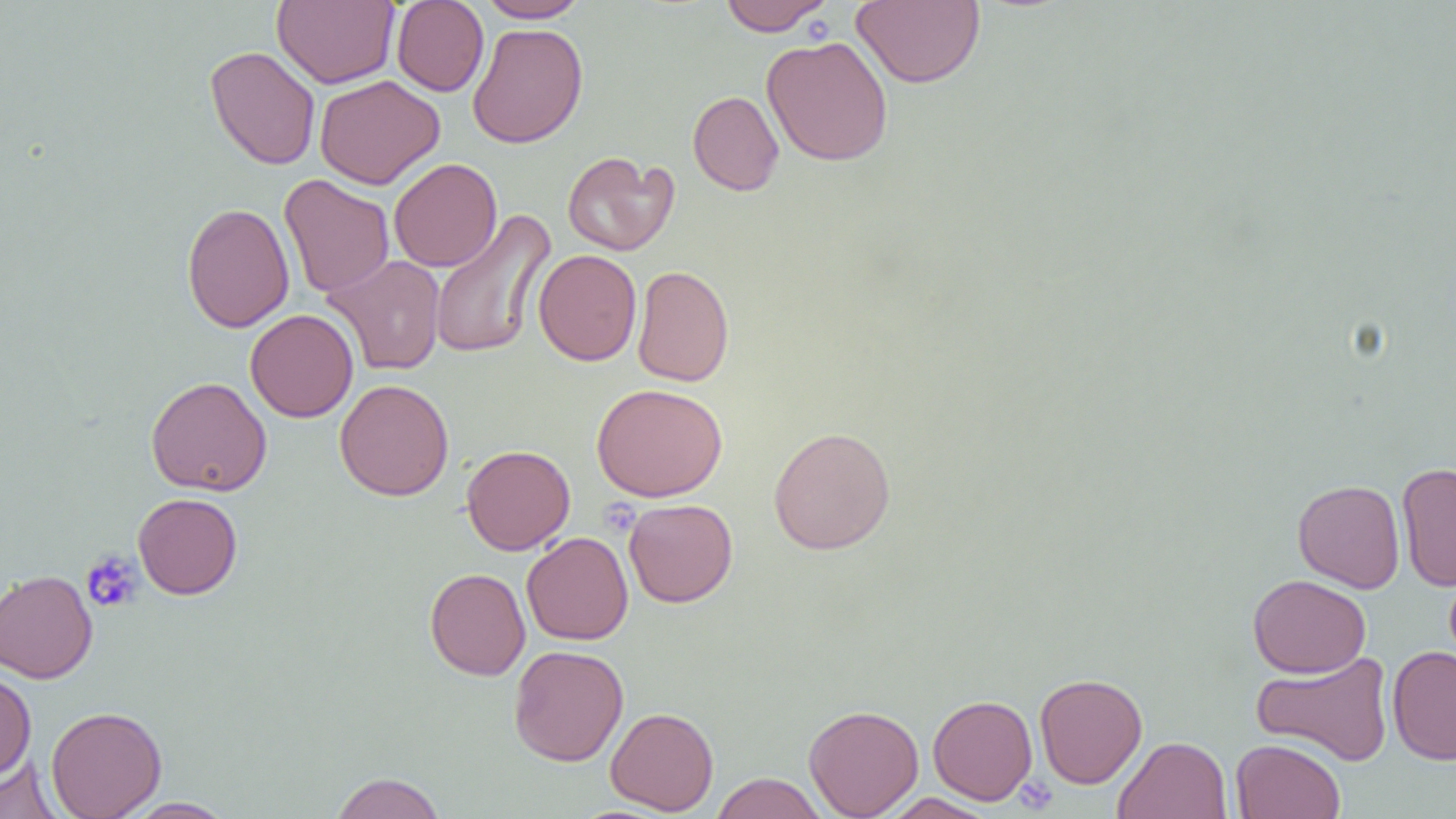
Approximate bounding boxes as named x1/y1/x2/y2 corners in pixels. Platelet locations: (x1=80, y1=550, x2=143, y2=614), (x1=1014, y1=776, x2=1058, y2=813). Uninfected red blood cell locations: (x1=272, y1=0, x2=399, y2=88), (x1=476, y1=0, x2=591, y2=22), (x1=718, y1=0, x2=835, y2=35), (x1=852, y1=0, x2=985, y2=88), (x1=391, y1=1, x2=489, y2=97), (x1=467, y1=22, x2=588, y2=148), (x1=762, y1=35, x2=893, y2=166), (x1=205, y1=46, x2=320, y2=170), (x1=315, y1=75, x2=445, y2=189), (x1=687, y1=90, x2=784, y2=196), (x1=562, y1=150, x2=677, y2=256), (x1=389, y1=158, x2=502, y2=272), (x1=279, y1=174, x2=394, y2=298), (x1=181, y1=202, x2=294, y2=333), (x1=429, y1=209, x2=556, y2=361), (x1=533, y1=249, x2=642, y2=366), (x1=323, y1=254, x2=446, y2=377), (x1=632, y1=265, x2=734, y2=387), (x1=245, y1=308, x2=358, y2=423), (x1=146, y1=376, x2=272, y2=496), (x1=335, y1=378, x2=454, y2=501), (x1=591, y1=382, x2=728, y2=502), (x1=768, y1=425, x2=896, y2=555), (x1=461, y1=444, x2=575, y2=555), (x1=1396, y1=461, x2=1456, y2=591), (x1=1293, y1=479, x2=1405, y2=593), (x1=133, y1=493, x2=243, y2=599), (x1=623, y1=498, x2=738, y2=607), (x1=522, y1=532, x2=634, y2=645), (x1=424, y1=568, x2=530, y2=680), (x1=0, y1=569, x2=98, y2=683), (x1=1247, y1=574, x2=1371, y2=678), (x1=509, y1=645, x2=628, y2=766), (x1=1387, y1=645, x2=1456, y2=765), (x1=1252, y1=651, x2=1395, y2=766), (x1=0, y1=669, x2=36, y2=781), (x1=1034, y1=672, x2=1147, y2=788), (x1=928, y1=694, x2=1037, y2=805), (x1=803, y1=704, x2=923, y2=818), (x1=46, y1=706, x2=167, y2=818), (x1=606, y1=707, x2=719, y2=815), (x1=1113, y1=736, x2=1233, y2=819), (x1=1231, y1=738, x2=1345, y2=819), (x1=0, y1=755, x2=64, y2=819), (x1=329, y1=772, x2=446, y2=819), (x1=711, y1=772, x2=828, y2=819), (x1=881, y1=793, x2=998, y2=818), (x1=122, y1=797, x2=236, y2=818). Slide-level diagnosis: negative for blood parasites. Single field of view. 1000x magnification. Thin blood smear. Image is 1456×819 pixels. Optical microscopy.